Classify this cell by malaria status.
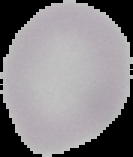

Uninfected.

{
  "image_type": "segmented cell region with the area outside set to black",
  "image_size": "133×157 pixels",
  "preparation": "thin blood smear"
}